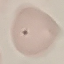

Summary:
  - Malaria status: uninfected
  - Stain: Giemsa
  - Capture: smartphone through the microscope eyepiece
  - Preparation: thin smear
  - Image type: automatically extracted cell patch, resized to 64 × 64 pixels